Report the malaria status of this cell.
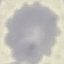
It is uninfected.

Summary:
  - Image type: automatically extracted cell patch, resized to 64 × 64 pixels
  - Preparation: thin blood film
  - Stain: Giemsa
  - Capture: smartphone camera at the microscope eyepiece